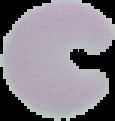
{
  "image_type": "segmented cell region on a black background",
  "image_size": "115×121 pixels",
  "result": "no malaria parasites detected",
  "preparation": "thin blood film"
}